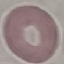

Result: negative for malaria parasites. Giemsa-stained preparation. Thin blood smear. Photographed with a smartphone camera at the microscope eyepiece. Automatically extracted cell patch, resized to 64 × 64 pixels.